Identify the parasite.
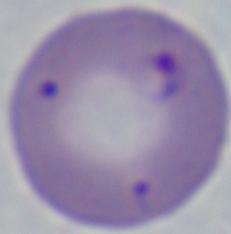
Babesia.

modality = micrograph
magnification = 1000x